Classify this cell by malaria status.
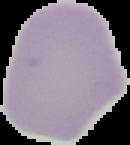
It is uninfected.

image size = 130×145 pixels
image type = cell region segmented out of the field of view; surrounding area masked to black
preparation = thin blood film